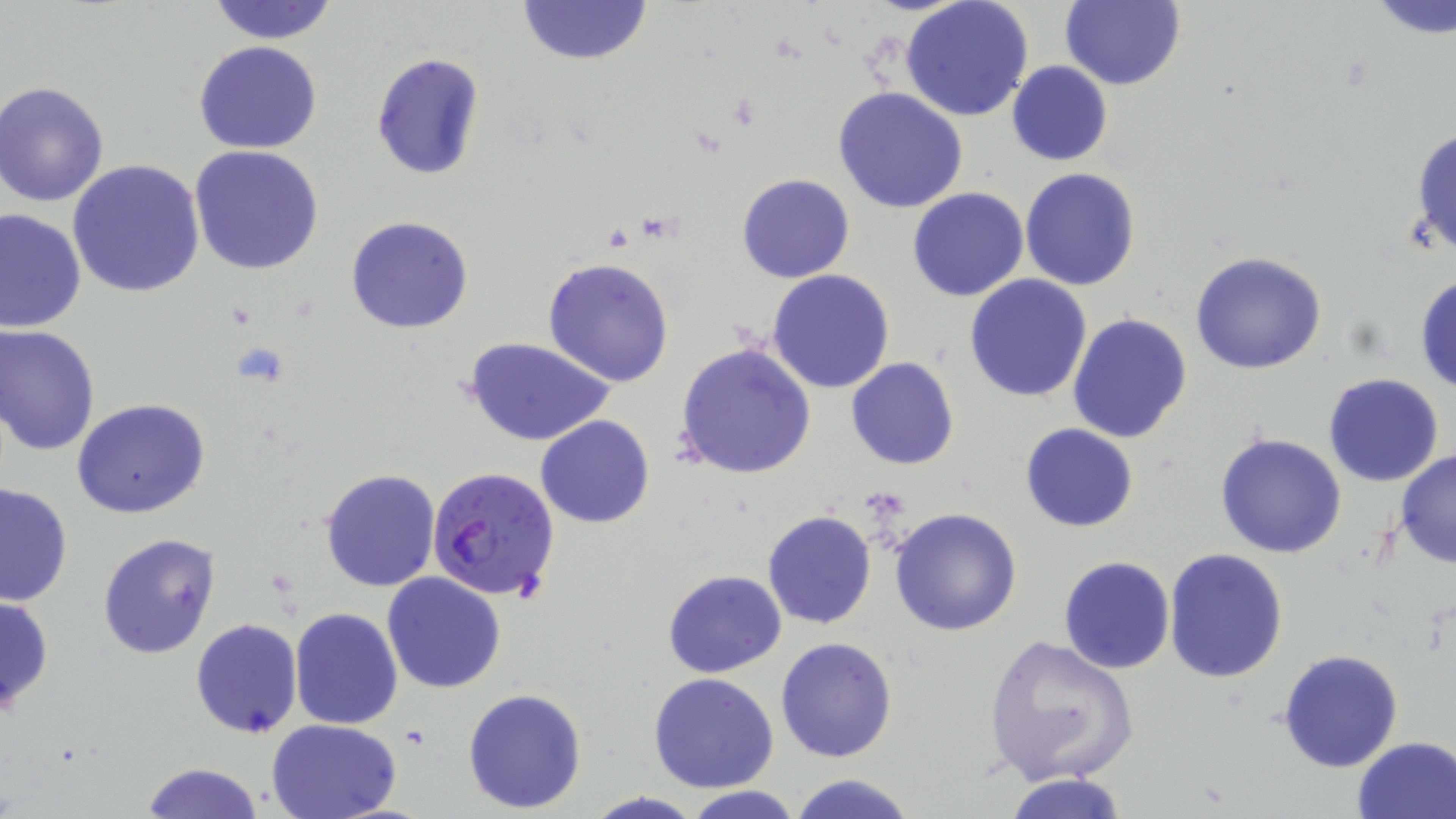

Summary:
  - Coordinate format: approximate bounding boxes as (x1, y1, x2, y2) in pixels
  - Uninfected red blood cell locations: (204, 0, 341, 44), (518, 0, 653, 66), (901, 0, 1035, 122), (1060, 0, 1184, 90), (1366, 1, 1456, 39), (192, 40, 323, 154), (370, 53, 485, 179), (1007, 60, 1114, 165), (1, 81, 113, 207), (833, 87, 967, 213), (1409, 124, 1456, 261), (189, 145, 326, 275), (66, 160, 207, 300), (1020, 167, 1141, 292), (737, 173, 854, 283), (908, 187, 1029, 302), (1, 207, 87, 332), (345, 213, 475, 334), (1190, 251, 1330, 374), (543, 258, 675, 386), (768, 269, 893, 393), (1415, 272, 1456, 397), (964, 275, 1093, 403), (1066, 312, 1195, 445), (1, 324, 100, 456), (463, 336, 614, 448), (675, 342, 816, 480), (847, 358, 959, 471), (1323, 373, 1444, 488), (72, 398, 211, 520), (536, 414, 655, 528), (1019, 421, 1140, 532), (1215, 433, 1347, 558), (1393, 450, 1456, 569), (319, 467, 441, 592), (0, 480, 72, 607), (889, 506, 1022, 635), (762, 508, 877, 630), (97, 532, 222, 659), (1164, 549, 1289, 682), (1058, 556, 1176, 674), (661, 569, 786, 678), (382, 572, 508, 695), (0, 593, 54, 718), (290, 607, 403, 729), (190, 618, 304, 738), (983, 633, 1142, 788), (775, 636, 898, 762), (1277, 649, 1404, 773), (648, 673, 779, 793), (462, 687, 587, 814), (266, 718, 406, 818), (1352, 735, 1456, 818), (138, 761, 264, 819), (790, 772, 916, 819), (1005, 772, 1129, 819), (678, 785, 805, 819), (581, 792, 706, 819)
  - Plasmodium falciparum-infected red blood cell locations: (425, 466, 558, 602)
  - Slide-level diagnosis: Plasmodium falciparum
  - Modality: optical microscopy
  - Magnification: 1000x
  - Stain: May-Grünwald-Giemsa
  - Preparation: thin blood smear
  - Field of view: single
  - Image size: 1456×819 pixels